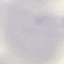
result = no malaria parasites detected
preparation = thin smear
image type = automatically extracted cell patch, resized to 64 × 64 pixels
capture = smartphone camera at the microscope eyepiece
stain = Giemsa